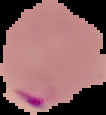

image type = segmented cell region on a black background
result = malaria parasites detected
preparation = thin blood smear
image size = 106×115 pixels